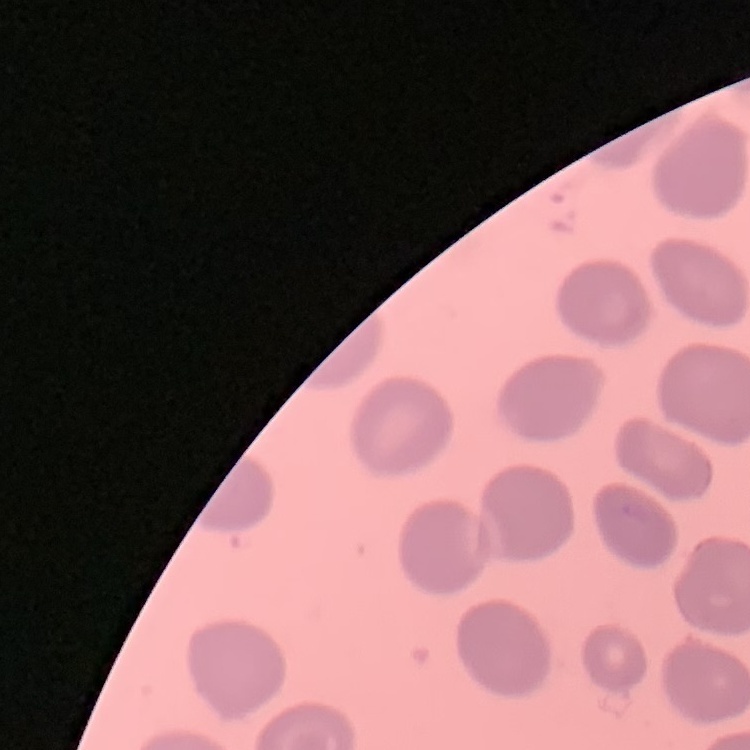
{
  "erythrocyte_morphology": "no rouleaux formation",
  "preparation": "thin peripheral smear",
  "image_type": "one tile cut from a larger photomicrograph",
  "stain": "Field's or Giemsa"
}